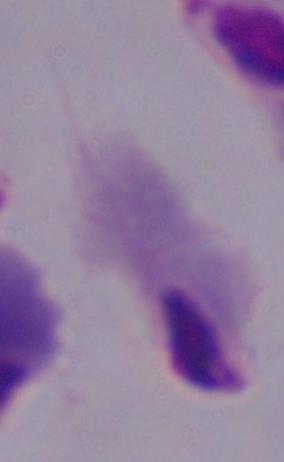

Summary:
  - Magnification: 1000x
  - Identification: trichomonad
  - Modality: photomicrograph